Locate every malaria parasite.
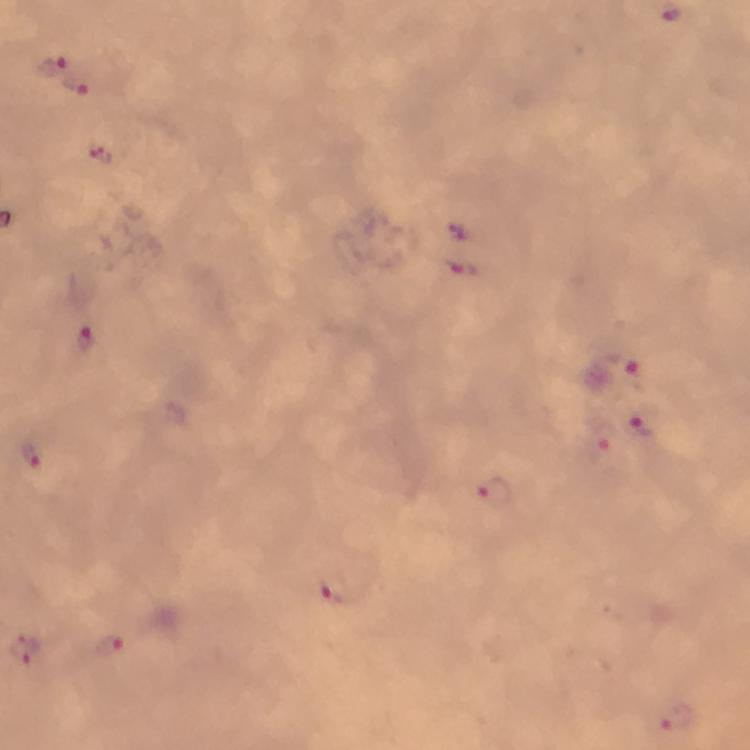
Approximate centers as (x, y) in pixels.
Malaria parasites: (52, 65), (78, 87), (462, 268), (88, 335), (623, 368), (640, 423), (599, 450), (32, 453), (493, 496), (333, 587), (111, 647), (679, 717).

Thick blood smear. Cropped region of a single field of view. At 100x magnification. Immersion oil was used. Photographed with a smartphone mounted on the microscope. From a malaria diagnostic workup. Giemsa stain. Image is 750×750 pixels.